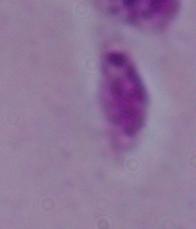
A Leishmania parasite is shown. Photomicrograph. 1000x magnification.